Assess this cell for malaria.
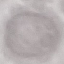

Uninfected.

Summary:
  - Stain: Giemsa
  - Preparation: thin blood film
  - Image type: automatically extracted cell patch, resized to 64 × 64 pixels
  - Capture: smartphone camera at the microscope eyepiece